Locate every blood parasite and identify its species.
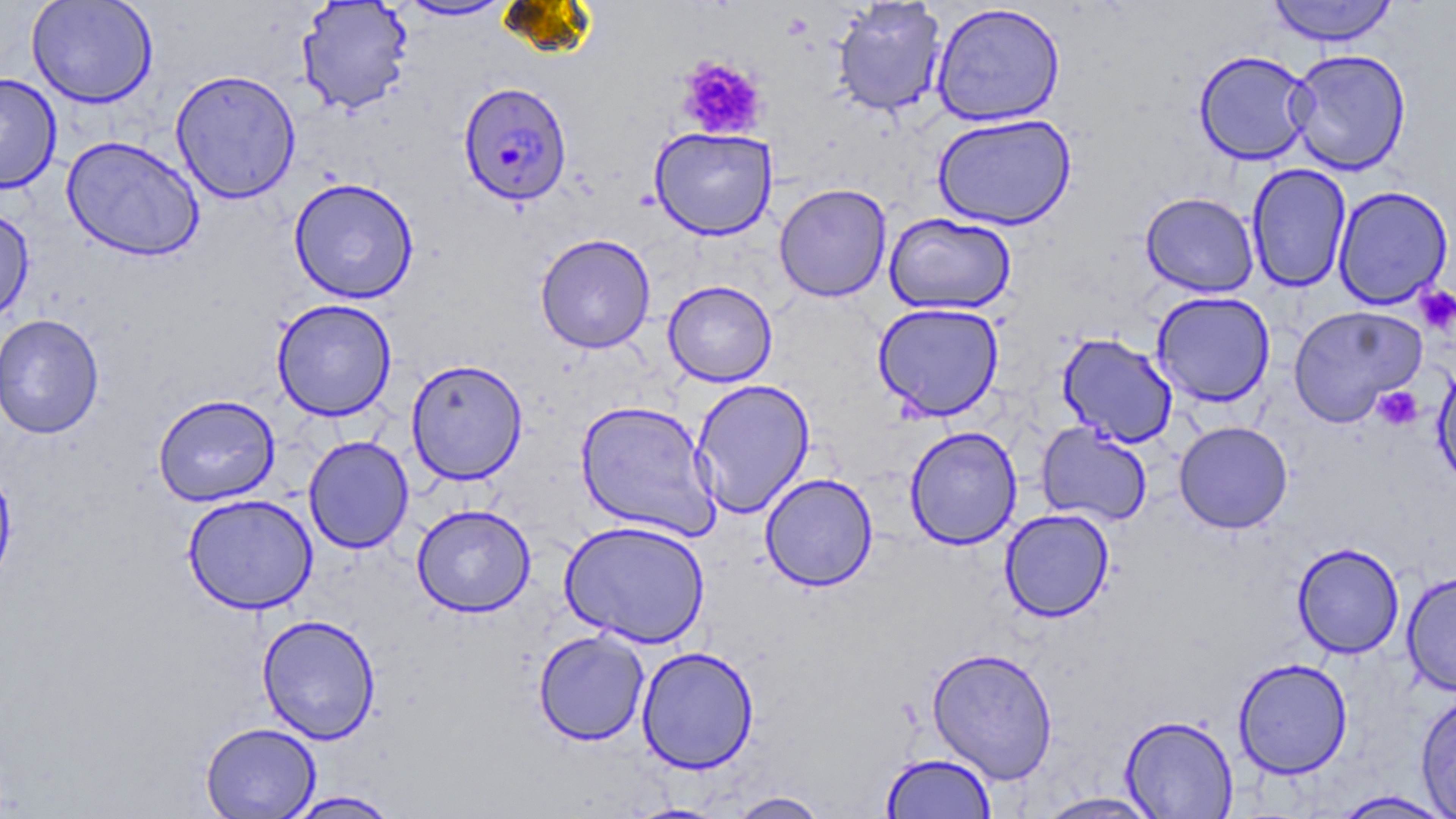

Approximate bounding boxes as named x1/y1/x2/y2 corners in pixels.
Plasmodium falciparum-infected red blood cells: (x1=457, y1=82, x2=573, y2=205).
No Plasmodium ovale, Plasmodium malariae, Plasmodium vivax, Babesia divergens, or Trypanosoma brucei observed.

Summary:
  - Uninfected red blood cell locations: (x1=26, y1=0, x2=158, y2=108), (x1=296, y1=0, x2=415, y2=115), (x1=397, y1=0, x2=514, y2=21), (x1=1267, y1=0, x2=1398, y2=46), (x1=830, y1=1, x2=947, y2=117), (x1=930, y1=3, x2=1067, y2=127), (x1=1286, y1=48, x2=1412, y2=176), (x1=1194, y1=49, x2=1313, y2=165), (x1=170, y1=69, x2=301, y2=203), (x1=0, y1=73, x2=62, y2=194), (x1=933, y1=113, x2=1076, y2=230), (x1=649, y1=127, x2=778, y2=240), (x1=61, y1=136, x2=204, y2=261), (x1=1245, y1=163, x2=1352, y2=293), (x1=288, y1=177, x2=419, y2=304), (x1=774, y1=183, x2=892, y2=303), (x1=1332, y1=185, x2=1454, y2=310), (x1=1140, y1=192, x2=1260, y2=297), (x1=0, y1=205, x2=35, y2=327), (x1=884, y1=212, x2=1017, y2=315), (x1=535, y1=233, x2=656, y2=353), (x1=663, y1=280, x2=777, y2=387), (x1=1151, y1=290, x2=1276, y2=407), (x1=271, y1=298, x2=397, y2=421), (x1=872, y1=302, x2=1005, y2=421), (x1=1288, y1=304, x2=1427, y2=428), (x1=0, y1=314, x2=104, y2=439), (x1=1057, y1=332, x2=1179, y2=448), (x1=406, y1=358, x2=528, y2=485), (x1=1432, y1=359, x2=1456, y2=491), (x1=691, y1=378, x2=815, y2=518), (x1=153, y1=394, x2=280, y2=506), (x1=575, y1=400, x2=720, y2=541), (x1=1174, y1=420, x2=1293, y2=534), (x1=1036, y1=422, x2=1152, y2=527), (x1=904, y1=426, x2=1022, y2=550), (x1=304, y1=435, x2=414, y2=554), (x1=760, y1=472, x2=878, y2=591), (x1=182, y1=493, x2=319, y2=614), (x1=412, y1=504, x2=536, y2=617), (x1=1000, y1=508, x2=1114, y2=622), (x1=559, y1=520, x2=711, y2=648), (x1=1292, y1=542, x2=1404, y2=658), (x1=1401, y1=571, x2=1456, y2=696), (x1=257, y1=614, x2=381, y2=744), (x1=534, y1=629, x2=649, y2=745), (x1=636, y1=646, x2=759, y2=774), (x1=926, y1=646, x2=1058, y2=784), (x1=1233, y1=658, x2=1353, y2=779), (x1=1415, y1=691, x2=1456, y2=819), (x1=1121, y1=715, x2=1238, y2=818), (x1=201, y1=722, x2=320, y2=818), (x1=881, y1=753, x2=996, y2=819), (x1=1330, y1=790, x2=1455, y2=818), (x1=283, y1=791, x2=402, y2=818), (x1=726, y1=791, x2=831, y2=819), (x1=1034, y1=792, x2=1166, y2=818), (x1=621, y1=802, x2=732, y2=818)
  - Platelet locations: (x1=676, y1=55, x2=769, y2=140), (x1=1415, y1=285, x2=1456, y2=334), (x1=1373, y1=385, x2=1423, y2=431)
  - Slide-level diagnosis: Plasmodium falciparum
  - Image size: 1456×819 pixels
  - Magnification: 1000x
  - Modality: light microscopy
  - Field of view: one of a larger specimen
  - Stain: May-Grünwald-Giemsa
  - Preparation: thin blood smear